Classify this cell by malaria status.
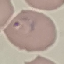
Parasitized.

Summary:
  - Preparation: thin blood smear
  - Image type: cell patch, automatically extracted from a larger field of view and resized to 64 × 64 pixels
  - Stain: Giemsa
  - Capture: smartphone camera at the microscope eyepiece